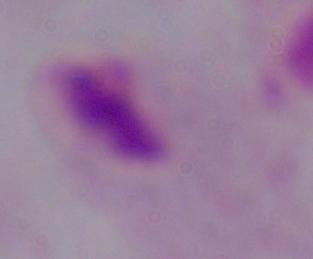
modality = micrograph
magnification = 1000x
identification = trichomonad